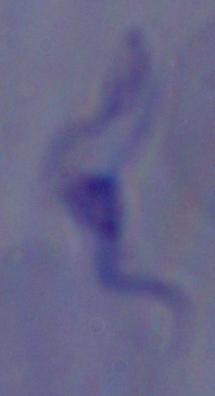

magnification = 1000x
identification = trypanosome
modality = photomicrograph